Report the malaria status of this cell.
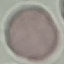

It is uninfected.

{
  "stain": "Giemsa",
  "image_type": "automatically extracted cell patch, resized to 64 × 64 pixels",
  "preparation": "thin blood film",
  "capture": "smartphone camera at the microscope eyepiece"
}